Name the blood parasite species.
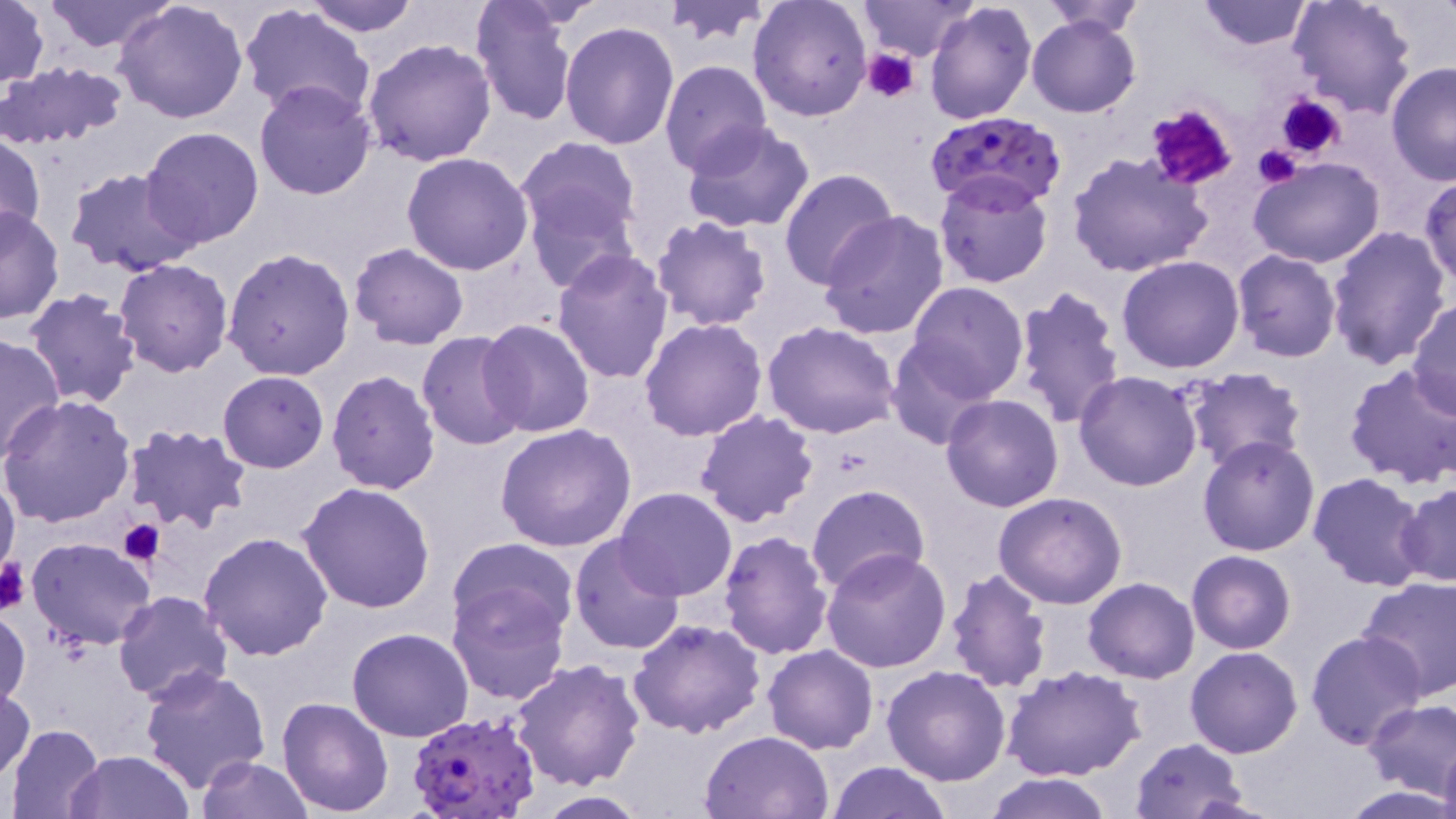

Plasmodium falciparum.

Summary:
  - Coordinate format: approximate bounding boxes as (x1,y1)-(x2,y2) corner pairs in pixels
  - Plasmodium falciparum-infected red blood cell locations: (925,112)-(1065,211), (406,710)-(542,819)
  - Platelet locations: (862,49)-(922,103), (1276,93)-(1346,159), (1143,103)-(1237,190), (1252,144)-(1304,188), (118,517)-(165,564), (0,553)-(28,616)
  - Uninfected red blood cell locations: (0,0)-(49,91), (41,0)-(176,52), (303,0)-(420,36), (662,0)-(773,45), (747,0)-(873,120), (857,0)-(980,63), (1039,0)-(1149,36), (1193,0)-(1317,50), (1288,0)-(1417,119), (112,1)-(248,124), (923,2)-(1037,125), (468,3)-(581,127), (238,4)-(373,121), (1028,13)-(1141,118), (559,20)-(681,150), (362,38)-(497,168), (659,59)-(774,178), (1386,61)-(1456,185), (0,62)-(129,150), (253,80)-(378,201), (1275,91)-(1357,159), (680,119)-(816,236), (139,127)-(265,249), (0,131)-(45,245), (515,136)-(644,249), (401,153)-(534,275), (1068,153)-(1212,279), (1248,157)-(1389,270), (63,167)-(202,277), (778,167)-(896,290), (934,172)-(1054,290), (1420,176)-(1456,289), (522,182)-(638,296), (0,206)-(64,324), (818,210)-(951,341), (649,215)-(774,331), (1325,225)-(1452,368), (349,241)-(469,349), (222,245)-(356,380), (552,247)-(675,383), (1231,251)-(1343,363), (1116,255)-(1245,373), (115,258)-(234,376), (904,282)-(1029,401), (1010,287)-(1127,430), (23,288)-(142,408), (1406,300)-(1456,417), (639,318)-(769,441), (478,319)-(596,439), (761,320)-(901,440), (0,332)-(65,466), (417,332)-(529,451), (886,342)-(998,449), (1344,362)-(1456,490), (1181,366)-(1308,477), (326,370)-(442,495), (217,371)-(330,473), (1074,372)-(1203,492), (0,394)-(136,527), (941,394)-(1065,512), (695,411)-(820,528), (495,422)-(638,554), (122,425)-(252,535), (1197,436)-(1321,556), (1307,473)-(1429,591), (0,476)-(19,582), (297,482)-(438,614), (1397,482)-(1456,587), (805,484)-(930,595), (614,488)-(738,602), (992,492)-(1127,609), (717,531)-(833,661), (198,532)-(333,662), (570,534)-(687,657), (26,536)-(157,650), (448,538)-(579,641), (821,548)-(951,674), (1187,550)-(1295,654), (945,568)-(1053,693), (1359,575)-(1456,700), (1082,578)-(1200,683), (447,586)-(570,705), (114,591)-(234,705), (0,606)-(30,711), (629,619)-(766,736), (347,628)-(474,742), (1306,630)-(1427,750), (296,642)-(427,788), (761,644)-(879,755), (1186,647)-(1302,759), (509,659)-(645,792), (140,663)-(271,793), (881,665)-(1013,786), (1002,667)-(1146,784), (0,685)-(35,781), (277,697)-(394,817), (1362,699)-(1456,802), (5,723)-(105,819), (700,729)-(835,819), (1128,738)-(1251,818), (1437,744)-(1456,819), (68,749)-(196,819), (197,756)-(312,819), (825,760)-(951,819), (981,772)-(1116,819), (1341,784)-(1455,817), (532,793)-(650,818)
  - Preparation: thin blood smear
  - Image size: 1456×819 pixels
  - Magnification: 1000x
  - Field of view: one of a larger specimen
  - Stain: May-Grünwald-Giemsa
  - Modality: optical microscopy